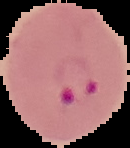 Malaria status: parasitized. Image is 130×148 pixels. From a thin blood film. Segmented cell region on a black background.